Assess this cell for malaria.
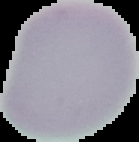

Uninfected.

Image is 139×142 pixels. Cell region segmented out of the field of view; the surrounding area is masked to black. From a thin blood film.